Comment on the morphology of the erythrocytes.
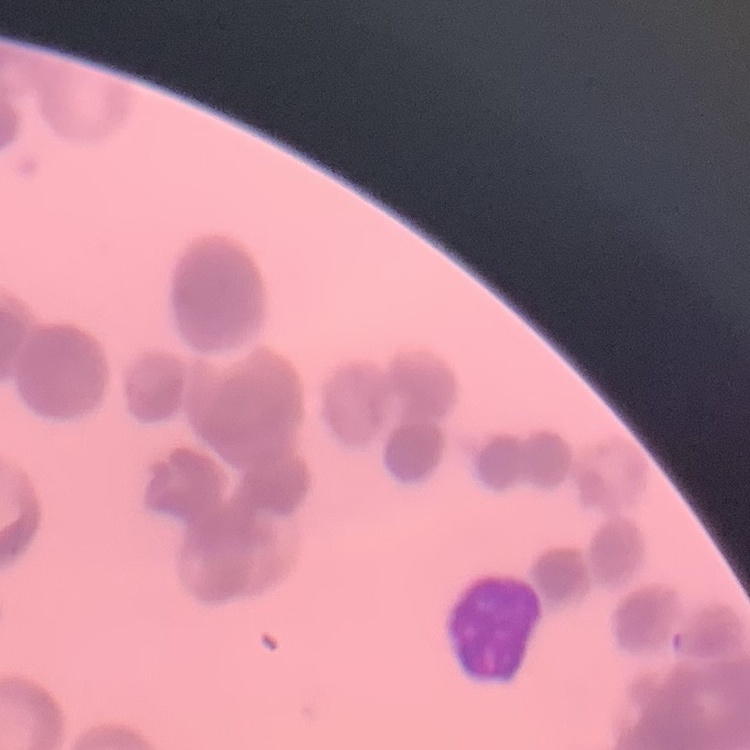

Rouleaux formation.

Summary:
  - Stain: Field's or Giemsa
  - Preparation: thin peripheral smear
  - Image type: square crop of a larger photomicrograph